Locate every leukocyte (white blood cell).
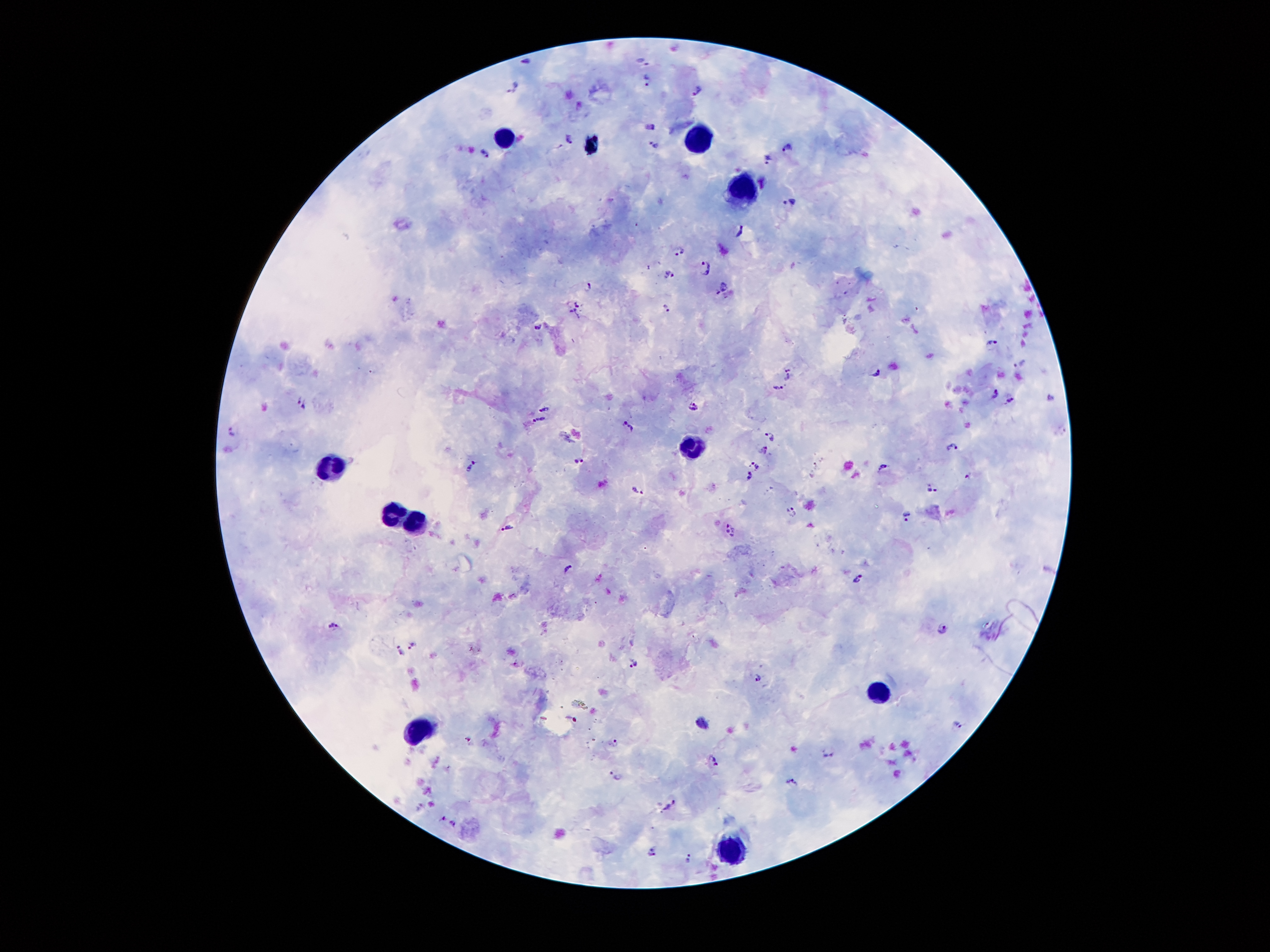

Approximate centers as [x, y] in pixels.
Leukocytes: [503, 132], [700, 132], [739, 196], [692, 448], [331, 468], [392, 515], [415, 521], [878, 689], [419, 732], [731, 846].

Malaria parasite locations: [641, 58], [526, 59], [647, 81], [513, 87], [697, 90], [649, 126], [568, 135], [652, 145], [787, 147], [485, 153], [767, 159], [791, 203], [741, 232], [678, 251], [707, 267], [669, 275], [589, 285], [722, 286], [578, 300], [667, 308], [572, 315], [538, 328], [993, 343], [1019, 363], [789, 373], [876, 374], [779, 389], [994, 395], [1051, 397], [297, 398], [1009, 399], [306, 406], [692, 406], [542, 410], [539, 420], [627, 424], [232, 430], [768, 434], [952, 446], [762, 450], [579, 457], [756, 464], [470, 467], [883, 467], [748, 477], [969, 477], [932, 487], [638, 490], [792, 512], [906, 515], [507, 528], [730, 532], [567, 565], [856, 580], [335, 624], [943, 632], [414, 644], [401, 654], [635, 661], [759, 674], [570, 719], [960, 723], [469, 738], [614, 742], [829, 752], [715, 761], [616, 774], [792, 779], [670, 804], [417, 806], [443, 818], [453, 824], [650, 851], [688, 858]. One field from this slide. Giemsa stain. 100x magnification. Patient malaria status: positive for Plasmodium falciparum. Smartphone photograph taken through the microscope eyepiece. Image is 1270×952 pixels. Thick peripheral-blood smear.